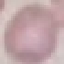

result = no malaria parasites detected
stain = Giemsa
image type = cell patch, automatically extracted from a larger field of view and resized to 64 × 64 pixels
preparation = thin blood smear
capture = smartphone camera at the microscope eyepiece